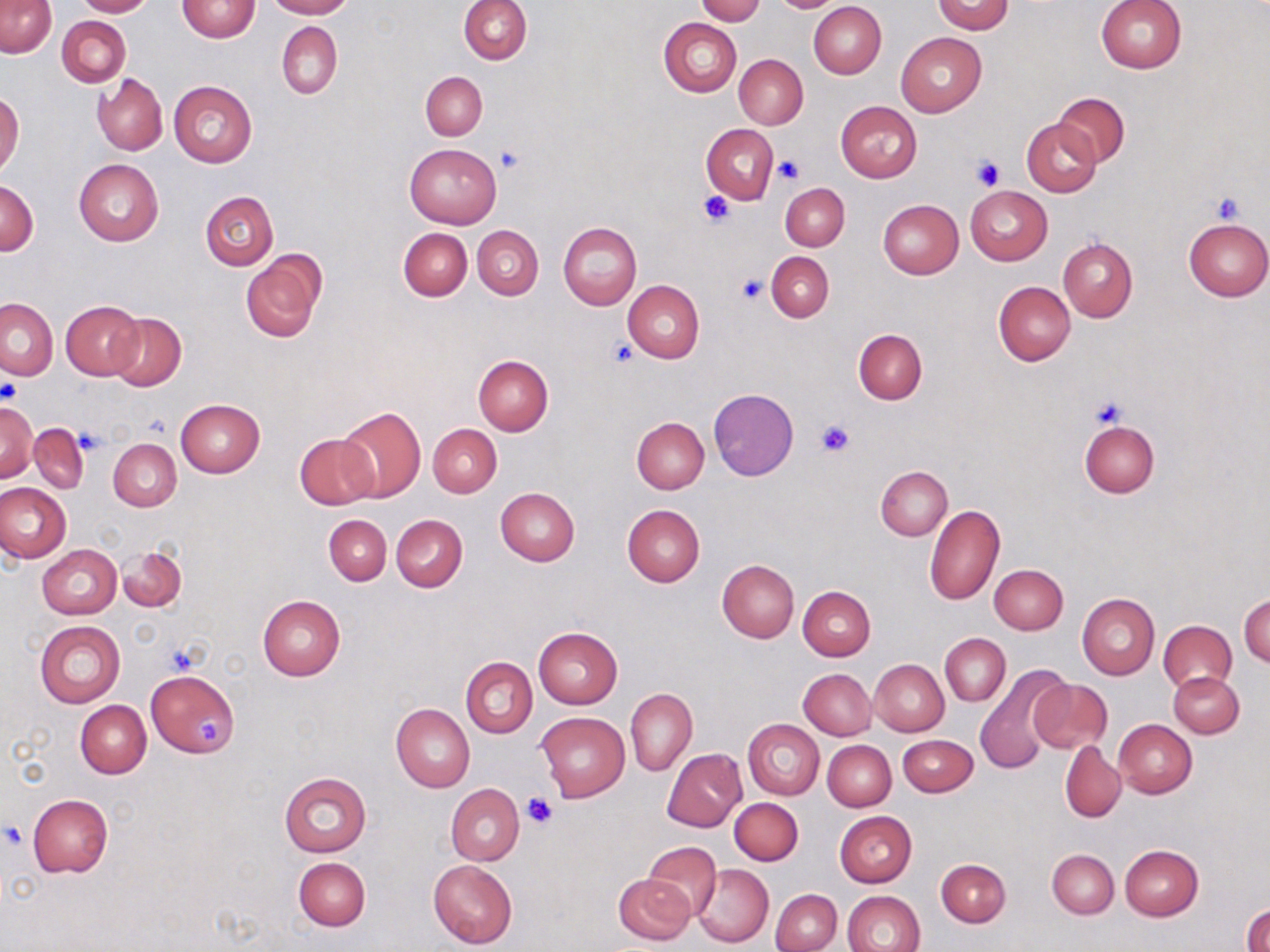
Summary:
  - Coordinate format: approximate bounding boxes as (x1, y1, x2, y2) in pixels
  - Uninfected red blood cell locations: (73, 0, 156, 16), (264, 0, 353, 18), (458, 0, 532, 64), (696, 0, 765, 24), (930, 0, 1013, 34), (177, 1, 259, 41), (772, 1, 840, 12), (1095, 1, 1186, 73), (1, 2, 56, 57), (808, 2, 887, 79), (57, 16, 130, 87), (659, 17, 742, 97), (277, 22, 341, 98), (896, 32, 986, 118), (734, 54, 808, 128), (421, 72, 487, 140), (93, 74, 167, 155), (169, 80, 256, 167), (0, 93, 24, 177), (1053, 93, 1129, 167), (835, 101, 922, 183), (1022, 118, 1101, 197), (702, 123, 778, 205), (404, 144, 501, 227), (74, 158, 164, 246), (1, 181, 38, 254), (780, 183, 849, 251), (965, 186, 1052, 266), (200, 191, 278, 271), (877, 199, 963, 278), (1183, 218, 1270, 300), (557, 222, 641, 310), (473, 225, 544, 299), (398, 228, 472, 301), (1059, 239, 1137, 321), (241, 251, 326, 344), (766, 251, 833, 323), (623, 280, 704, 363), (994, 281, 1075, 366), (1, 298, 58, 380), (60, 300, 144, 380), (107, 312, 186, 389), (854, 329, 926, 404), (473, 354, 553, 435), (708, 387, 798, 480), (175, 399, 265, 477), (0, 401, 37, 482), (337, 405, 426, 501), (2, 413, 67, 496), (632, 416, 709, 493), (1080, 419, 1159, 497), (29, 423, 88, 494), (428, 424, 501, 498), (294, 433, 380, 510), (109, 438, 181, 510), (876, 466, 952, 540), (0, 482, 71, 562), (495, 488, 579, 566), (622, 504, 704, 587), (924, 505, 1005, 605), (391, 514, 468, 592), (323, 515, 391, 585), (38, 544, 122, 619), (118, 545, 187, 612), (717, 559, 798, 642), (989, 564, 1067, 634), (798, 586, 875, 661), (1077, 593, 1159, 680), (257, 594, 346, 681), (1240, 595, 1269, 669), (35, 620, 126, 708), (1157, 620, 1236, 694), (532, 627, 622, 709), (941, 633, 1010, 707), (462, 656, 537, 738), (870, 659, 949, 736), (973, 665, 1073, 773), (798, 668, 876, 740), (146, 670, 239, 755), (1169, 671, 1243, 738), (1028, 679, 1112, 754), (626, 688, 697, 777), (75, 700, 152, 777), (391, 704, 474, 793), (535, 711, 630, 802), (743, 718, 825, 799), (1113, 719, 1196, 798), (898, 734, 978, 796), (823, 740, 895, 810), (1060, 741, 1125, 821), (662, 749, 747, 831), (279, 771, 371, 857), (447, 783, 524, 865), (27, 793, 113, 878), (729, 797, 804, 865), (835, 811, 917, 887), (642, 841, 721, 919), (1121, 845, 1203, 921), (1047, 849, 1119, 918), (294, 857, 370, 931), (936, 859, 1011, 927), (428, 860, 517, 947), (694, 864, 773, 947), (613, 872, 696, 945), (771, 889, 841, 952), (842, 891, 925, 952), (1245, 905, 1269, 952)
  - Platelet locations: (495, 145, 525, 175), (775, 155, 804, 185), (972, 155, 1004, 191), (699, 190, 736, 228), (1211, 194, 1244, 225), (736, 274, 766, 302), (608, 338, 638, 366), (1, 380, 22, 407), (1090, 394, 1129, 431), (815, 419, 855, 457), (75, 429, 106, 456), (195, 714, 225, 748), (521, 792, 556, 829), (3, 824, 24, 850)
  - Slide-level diagnosis: negative for blood parasites
  - Magnification: 1000x
  - Modality: optical microscopy
  - Preparation: thin blood smear
  - Image size: 1270×952 pixels
  - Stain: May-Grünwald-Giemsa
  - Field of view: one of a larger specimen